Locate every Plasmodium falciparum-infected red blood cell.
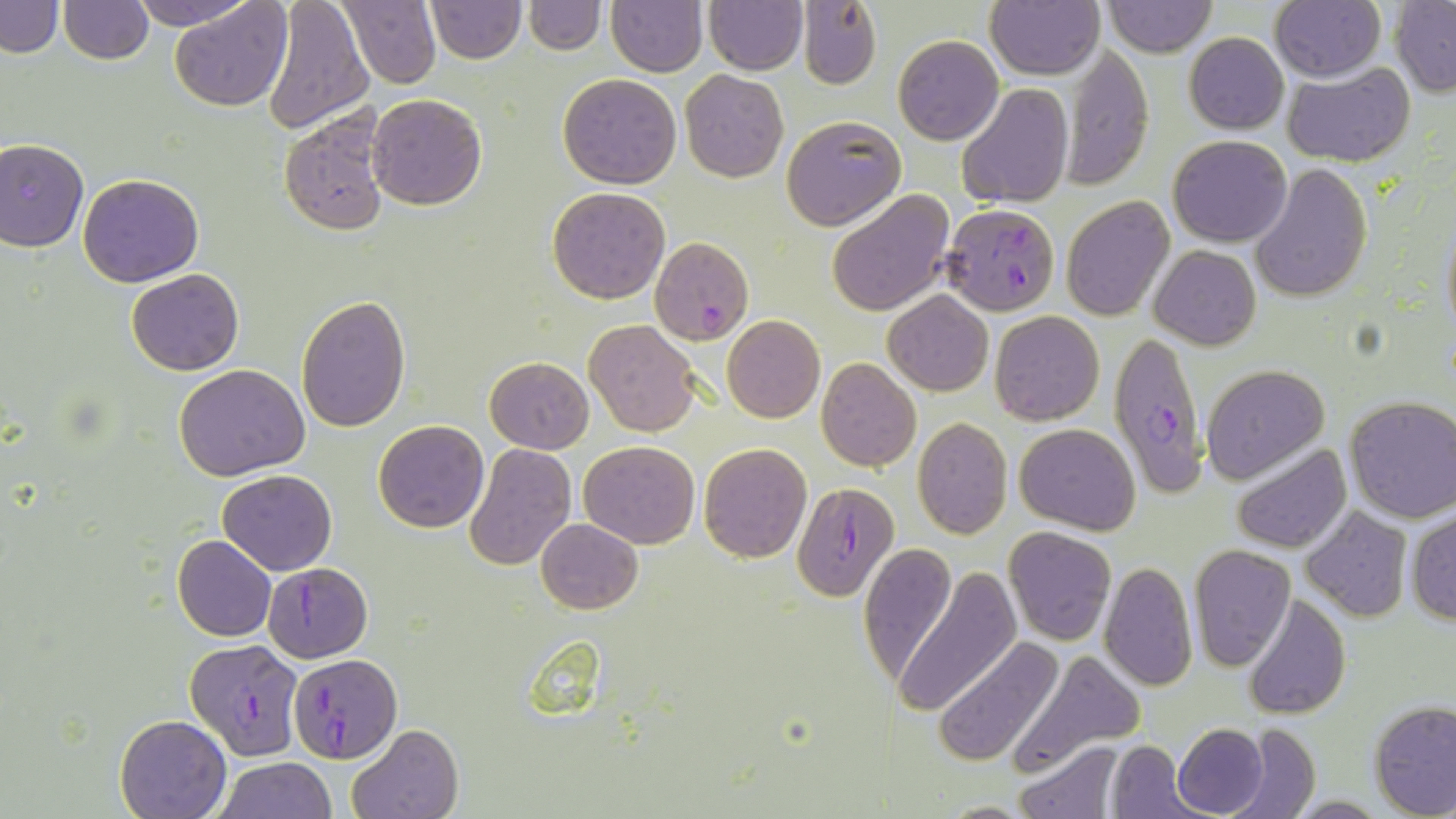
Approximate bounding boxes as (x1,y1)-(x2,y2) corner pairs in pixels.
Plasmodium falciparum-infected red blood cells: (941,202)-(1061,315), (651,238)-(754,346), (1108,327)-(1213,501), (790,479)-(899,599), (262,562)-(373,663), (186,637)-(307,761), (289,654)-(398,762).

slide-level diagnosis = Plasmodium falciparum
preparation = thin blood smear
field of view = single
uninfected red blood cell locations = approximate bounding boxes as (x1,y1)-(x2,y2) corner pairs in pixels: (1,0)-(64,57), (58,0)-(153,64), (127,0)-(258,30), (169,0)-(292,111), (261,0)-(375,135), (338,0)-(441,89), (426,0)-(525,63), (523,0)-(603,54), (606,0)-(708,76), (703,1)-(809,74), (1102,1)-(1216,56), (1391,1)-(1456,96), (986,2)-(1103,80), (1270,2)-(1386,82), (799,3)-(881,90), (893,34)-(1003,145), (1183,34)-(1288,133), (1060,45)-(1154,189), (1282,62)-(1415,167), (680,70)-(787,182), (556,73)-(682,190), (956,82)-(1071,210), (367,93)-(487,210), (278,108)-(394,236), (781,115)-(907,230), (1168,134)-(1292,246), (0,138)-(89,250), (1250,163)-(1371,303), (78,174)-(204,287), (547,186)-(670,304), (826,188)-(955,316), (1061,197)-(1174,321), (1439,214)-(1456,341), (1149,245)-(1261,350), (127,269)-(243,376), (883,291)-(993,396), (296,295)-(411,432), (989,311)-(1104,425), (721,315)-(825,423), (584,320)-(701,436), (484,357)-(595,453), (816,357)-(921,471), (174,364)-(311,480), (1200,364)-(1328,481), (1343,396)-(1456,523), (912,417)-(1012,539), (373,419)-(489,532), (1014,422)-(1140,534), (579,440)-(700,549), (463,442)-(577,571), (699,443)-(813,564), (1231,443)-(1352,554), (218,469)-(336,575), (1302,507)-(1413,622), (1407,509)-(1456,625), (536,518)-(643,614), (1003,525)-(1117,645), (172,535)-(276,641), (858,542)-(959,689), (1188,544)-(1296,670), (1098,561)-(1198,691), (893,567)-(1021,716), (1245,594)-(1352,720), (932,635)-(1066,768), (1015,647)-(1146,770), (1369,700)-(1456,818), (115,714)-(231,818), (1222,722)-(1322,819), (348,723)-(465,819), (1172,723)-(1270,818), (1015,739)-(1124,818), (1105,740)-(1195,817), (216,757)-(335,818), (937,799)-(1036,817)
stain = May-Grünwald-Giemsa
image size = 1456×819 pixels
magnification = 1000x
modality = light microscopy